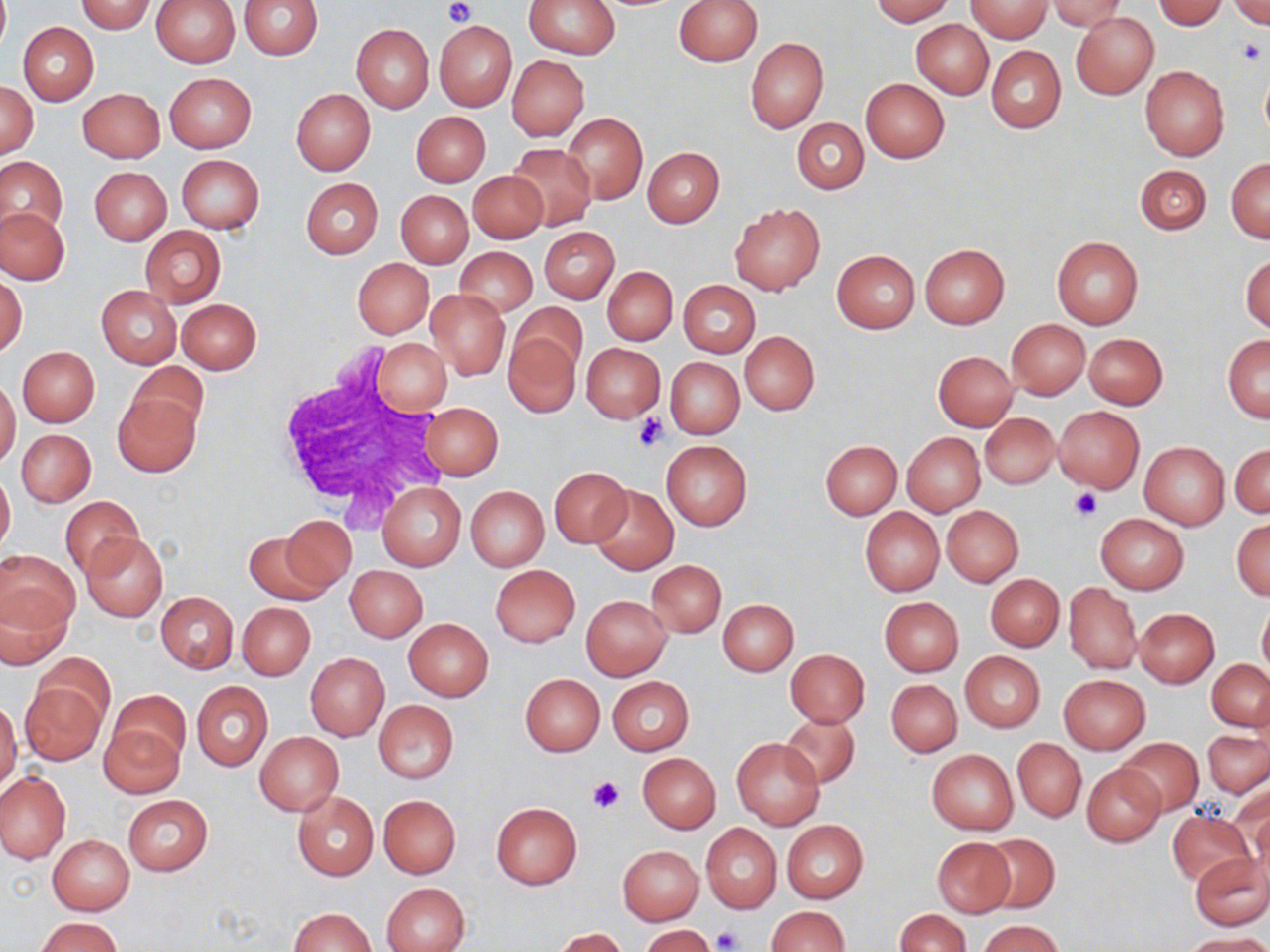

slide-level diagnosis = negative for blood parasites
platelet locations = approximate bounding boxes as (x1,y1)-(x2,y2) corner pairs in pixels: (443,0)-(474,25), (1236,37)-(1266,65), (632,411)-(668,453), (1070,488)-(1101,521), (588,775)-(624,814), (712,926)-(743,951)
uninfected red blood cell locations = approximate bounding boxes as (x1,y1)-(x2,y2) corner pairs in pixels: (0,0)-(9,53), (150,0)-(240,67), (240,0)-(322,59), (524,0)-(620,59), (673,0)-(763,66), (868,0)-(954,24), (967,0)-(1052,41), (1047,0)-(1125,31), (1153,0)-(1227,29), (74,1)-(156,33), (1230,1)-(1269,31), (1071,12)-(1159,99), (433,19)-(518,112), (911,19)-(994,99), (18,22)-(98,105), (351,23)-(434,112), (745,37)-(828,133), (986,44)-(1066,133), (507,55)-(588,140), (1139,65)-(1229,161), (1260,69)-(1270,141), (164,73)-(255,152), (861,79)-(949,163), (1,82)-(37,156), (78,88)-(165,162), (291,89)-(375,175), (411,111)-(490,186), (564,114)-(648,203), (792,118)-(868,194), (507,142)-(598,230), (643,146)-(724,227), (177,154)-(264,233), (0,156)-(66,241), (1226,157)-(1270,242), (1135,165)-(1212,235), (90,166)-(171,245), (468,170)-(547,242), (300,178)-(383,259), (395,190)-(473,268), (729,203)-(824,295), (1,207)-(69,285), (141,226)-(226,307), (539,226)-(619,303), (1052,236)-(1143,329), (920,243)-(1009,328), (455,247)-(537,317), (831,249)-(920,332), (1241,252)-(1269,334), (353,258)-(433,338), (602,266)-(677,345), (1,273)-(27,360), (678,280)-(760,358), (96,285)-(182,369), (425,290)-(510,380), (176,298)-(261,374), (512,302)-(587,378), (1007,320)-(1090,399), (504,331)-(580,416), (739,331)-(820,415), (1083,333)-(1167,409), (1224,335)-(1270,422), (372,338)-(451,416), (581,342)-(664,421), (18,346)-(100,426), (932,351)-(1018,430), (665,357)-(743,439), (128,361)-(208,437), (0,378)-(20,469), (112,393)-(201,478), (422,402)-(503,479), (1054,406)-(1144,492), (980,412)-(1060,488), (17,429)-(95,506), (902,433)-(985,516), (661,440)-(752,531), (820,440)-(901,519), (1138,440)-(1230,530), (1230,444)-(1269,518), (0,468)-(15,554), (550,468)-(632,546), (378,482)-(466,571), (588,484)-(679,576), (465,486)-(549,571), (60,496)-(143,580), (941,505)-(1024,587), (860,507)-(944,596), (1096,513)-(1188,594), (280,517)-(357,592), (1232,518)-(1270,601), (243,530)-(333,605), (80,532)-(168,621), (0,549)-(79,637), (647,560)-(727,637), (345,565)-(427,641), (490,565)-(580,646), (985,573)-(1065,651), (1063,582)-(1140,674), (1,584)-(73,667), (155,591)-(238,673), (581,595)-(672,680), (879,597)-(964,677), (1257,598)-(1270,680), (719,599)-(798,675), (237,601)-(315,680), (1134,608)-(1219,687), (403,618)-(494,702), (786,649)-(870,728), (960,651)-(1045,732), (37,653)-(115,733), (306,653)-(388,739), (1207,658)-(1269,731), (520,673)-(604,756), (1059,675)-(1150,753), (607,677)-(694,755), (886,680)-(961,756), (21,681)-(105,766), (191,682)-(272,771), (106,689)-(189,772), (0,698)-(22,794), (374,699)-(458,784), (780,713)-(859,788), (99,719)-(183,799), (1205,729)-(1269,797), (255,732)-(344,815), (1118,737)-(1203,816), (732,738)-(824,829), (1014,739)-(1085,822), (927,749)-(1018,834), (638,753)-(721,832), (1082,762)-(1166,846), (0,771)-(70,863), (1237,785)-(1270,868), (292,791)-(378,880), (122,794)-(213,875), (378,795)-(461,879), (491,802)-(581,889), (1167,810)-(1253,886), (782,819)-(868,903), (700,824)-(782,913), (980,833)-(1058,914), (48,835)-(134,914), (931,837)-(1015,917), (618,845)-(703,924), (1190,852)-(1269,929), (382,883)-(470,952), (765,906)-(849,952), (288,907)-(377,952), (895,909)-(969,952), (37,916)-(121,951), (977,920)-(1061,952), (640,924)-(716,952), (552,928)-(628,952), (1183,933)-(1270,952)
field of view = one of a larger specimen
preparation = thin blood smear
image size = 1270×952 pixels
magnification = 1000x
modality = light microscopy
white blood cell locations = approximate bounding boxes as (x1,y1)-(x2,y2) corner pairs in pixels: (269,350)-(449,523)
stain = May-Grünwald-Giemsa